Report the malaria status of this cell.
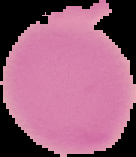
It is uninfected.

Segmented cell region on a black background. Image is 136×157 pixels. From a thin blood film.